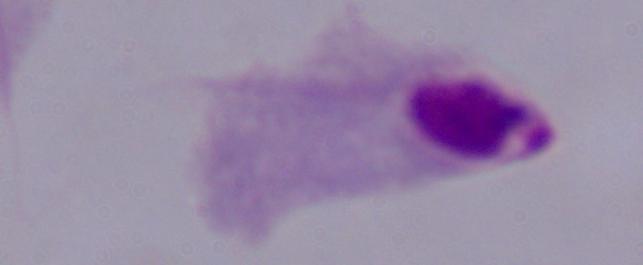
identification: trichomonad
magnification: 1000x
modality: photomicrograph